Point out each Plasmodium parasite.
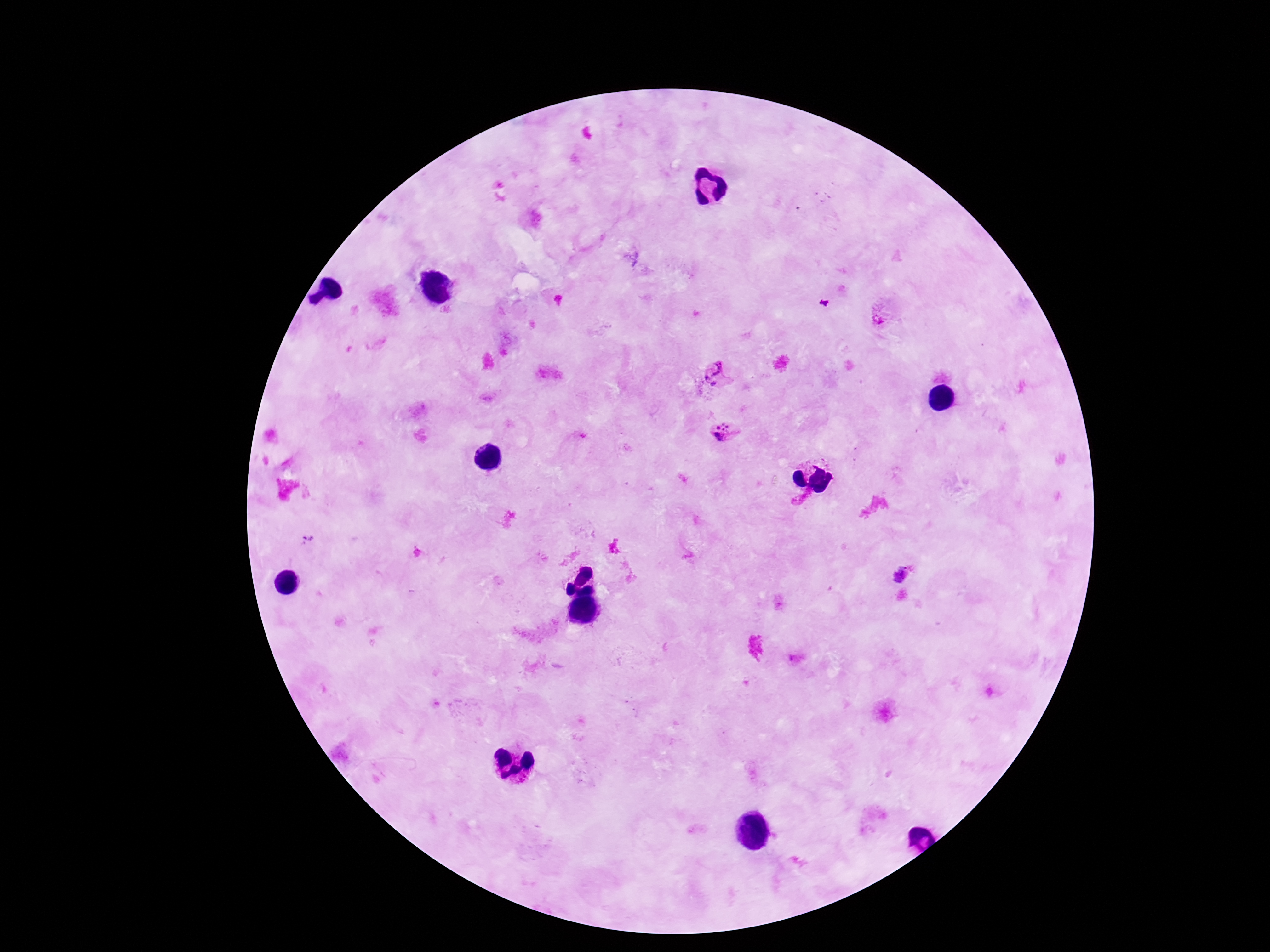
Approximate centers as [x, y] in pixels.
Plasmodium parasites: [879, 319], [716, 367], [706, 378], [713, 384], [723, 433], [901, 573].

Patient malaria status: positive. Single field of view. Thick blood smear. Giemsa stain. Smartphone photograph taken through the microscope eyepiece. 100x magnification. Image is 1270×952 pixels.